State which parasite is depicted.
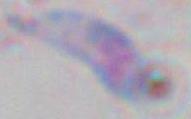

This is Toxoplasma gondii.

Summary:
  - Modality: micrograph
  - Magnification: 1000x